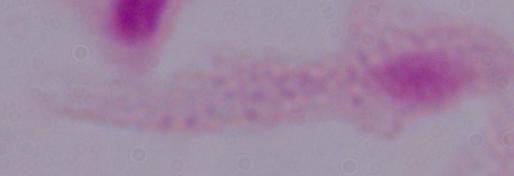
{
  "modality": "photomicrograph",
  "identification": "trichomonad",
  "magnification": "1000x"
}